Locate every leukocyte (white blood cell).
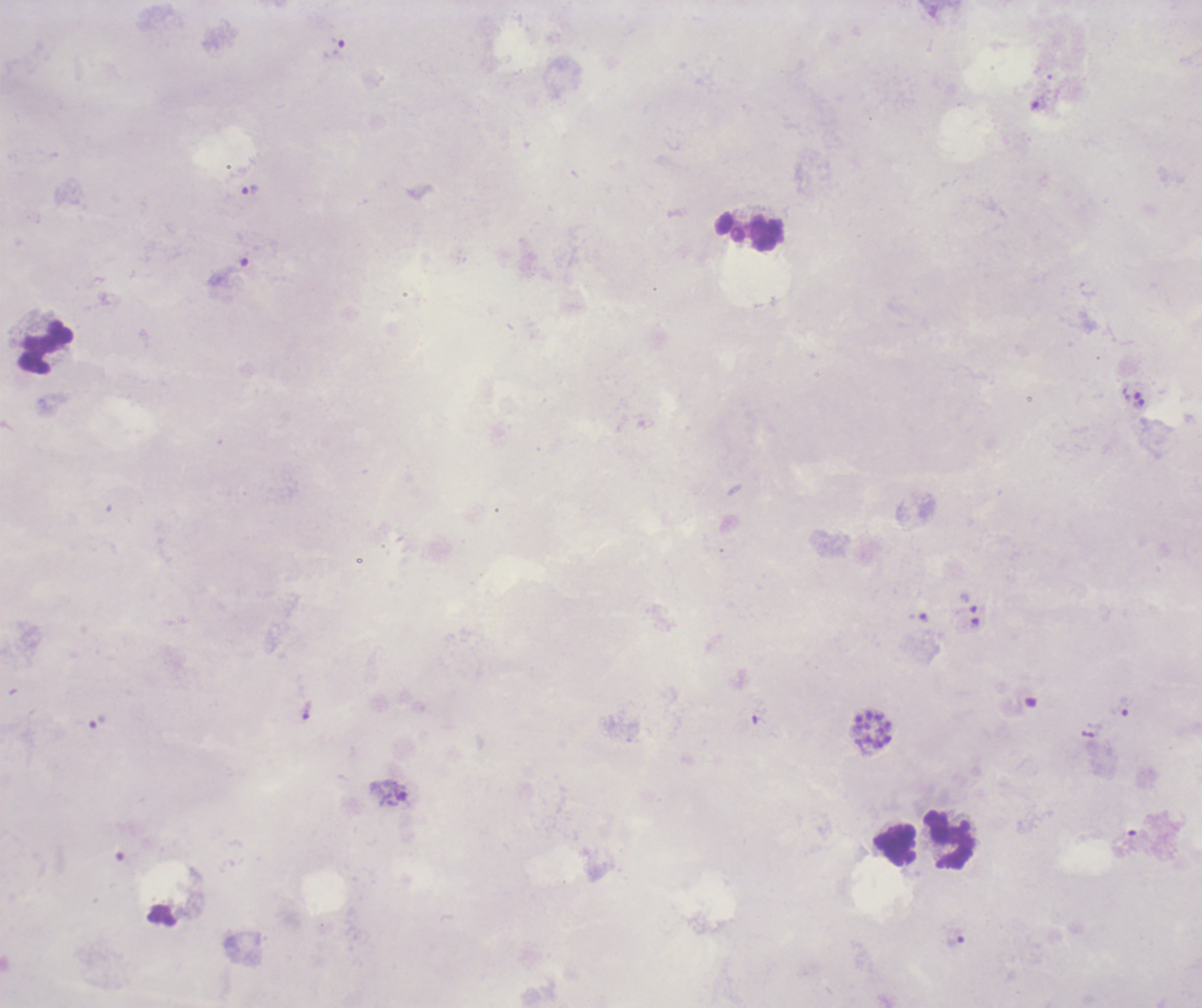

Approximate centers as (x, y) in pixels.
Leukocytes: (750, 231), (46, 347), (948, 838), (896, 846).

Approximate centers as (x, y) in pixels. Schizont locations: (874, 732). Trophozoite locations: (251, 191), (230, 272), (1138, 403), (1123, 707), (400, 792), (955, 937). Life-cycle stages observed: trophozoite, schizont. Previously used in a real diagnosis. Single field of view. Image is 1202×1008 pixels. Coloration quality: bad. 100x magnification. Result: positive for malaria parasites. Thick blood smear. Romanowsky-stained preparation. Background quality: unsatisfactory.